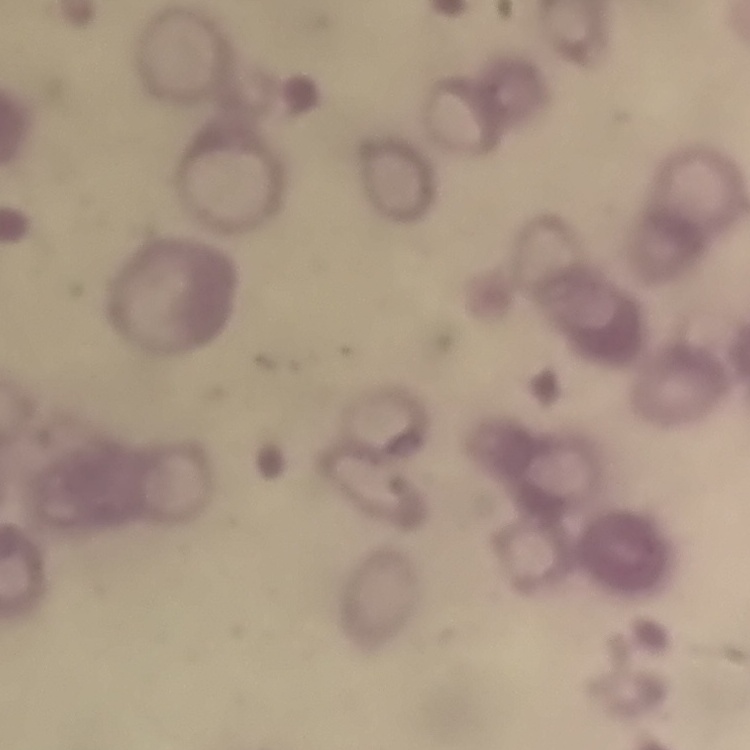

{
  "red_blood_cell_morphology": "rouleaux formation",
  "stain": "Field's or Giemsa",
  "image_type": "square crop of a larger photomicrograph",
  "preparation": "thin blood smear"
}